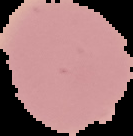
Malaria status: uninfected. Image is 133×136 pixels. From a thin blood film. Cell region segmented out of the field of view; the surrounding area is masked to black.